Classify this cell by malaria status.
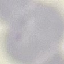

Uninfected.

Summary:
  - Image type: cell patch, automatically extracted from a larger field of view and resized to 64 × 64 pixels
  - Preparation: thin blood film
  - Capture: smartphone camera at the microscope eyepiece
  - Stain: Giemsa